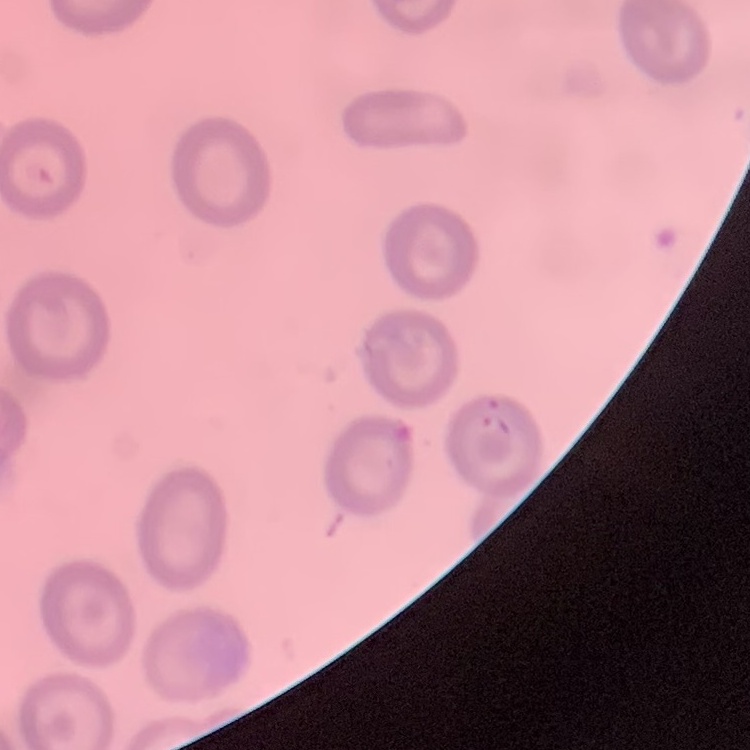 The erythrocytes show no rouleaux formation. Thin blood film. One tile cut from a larger photomicrograph. Stained with either Field's or Giemsa.